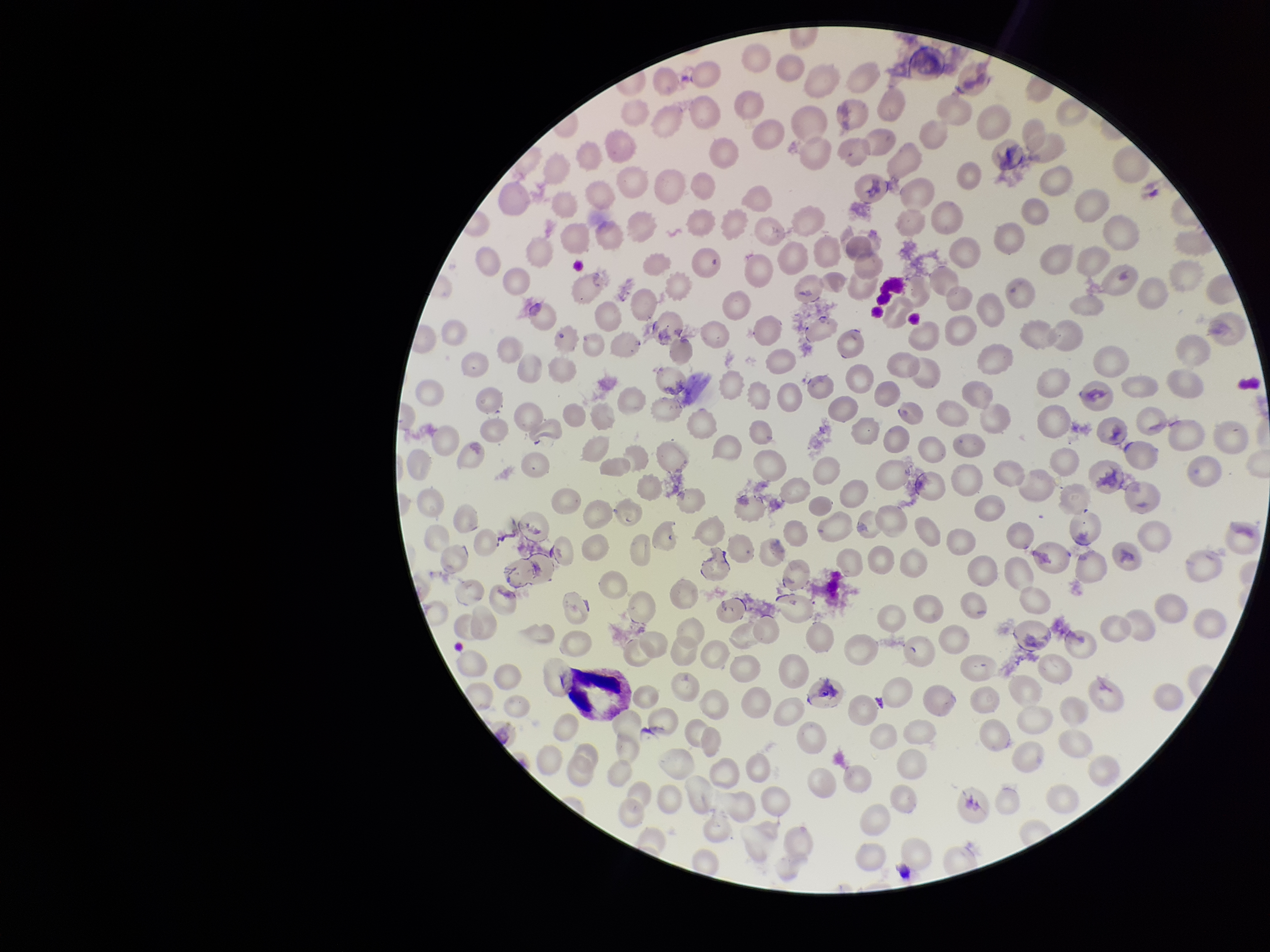

preparation = thin blood smear
species reported for this patient = Plasmodium vivax
parasitized red blood cell count = 0
patient malaria status = infected
stain = Giemsa
image size = 1270×952 pixels
parasitized red blood cells = none seen
capture = smartphone photograph through the microscope eyepiece
field of view = single
red blood cell count = 233